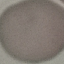
result: no malaria parasites seen
preparation: thin blood smear
image_type: automatically extracted cell patch, resized to 64 × 64 pixels
capture: smartphone camera at the microscope eyepiece
stain: Giemsa